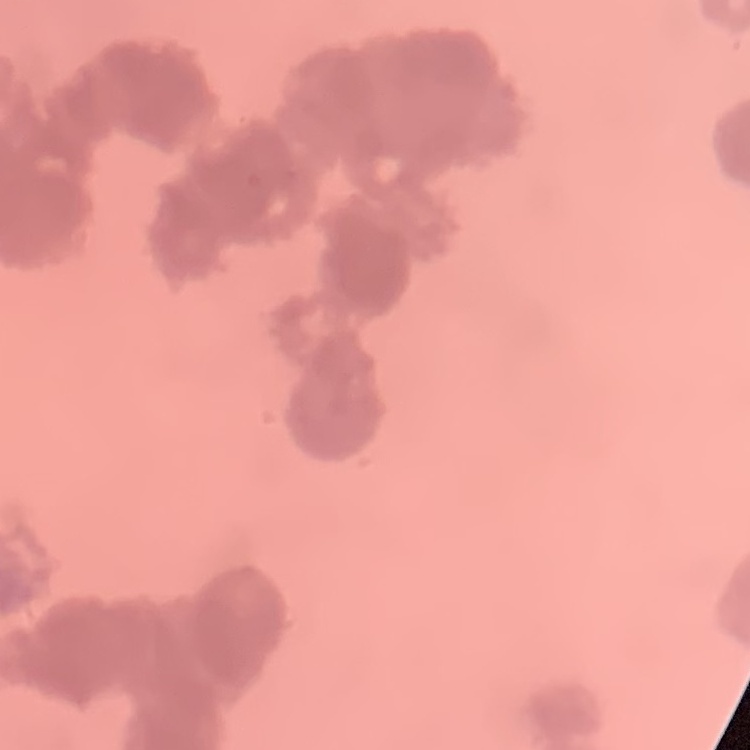
red_blood_cell_morphology: rouleaux formation
image_type: one tile cut from a larger photomicrograph
stain: Field's or Giemsa
preparation: thin blood film